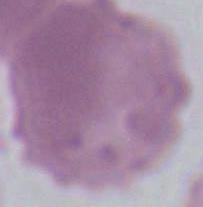 An erythrocyte is seen. Captured at 1000x magnification. Photomicrograph.